Assess this cell for malaria.
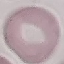
It is uninfected.

{
  "stain": "Giemsa",
  "image_type": "cell patch, automatically extracted from a larger field of view and resized to 64 × 64 pixels",
  "capture": "smartphone camera at the microscope eyepiece",
  "preparation": "thin blood film"
}